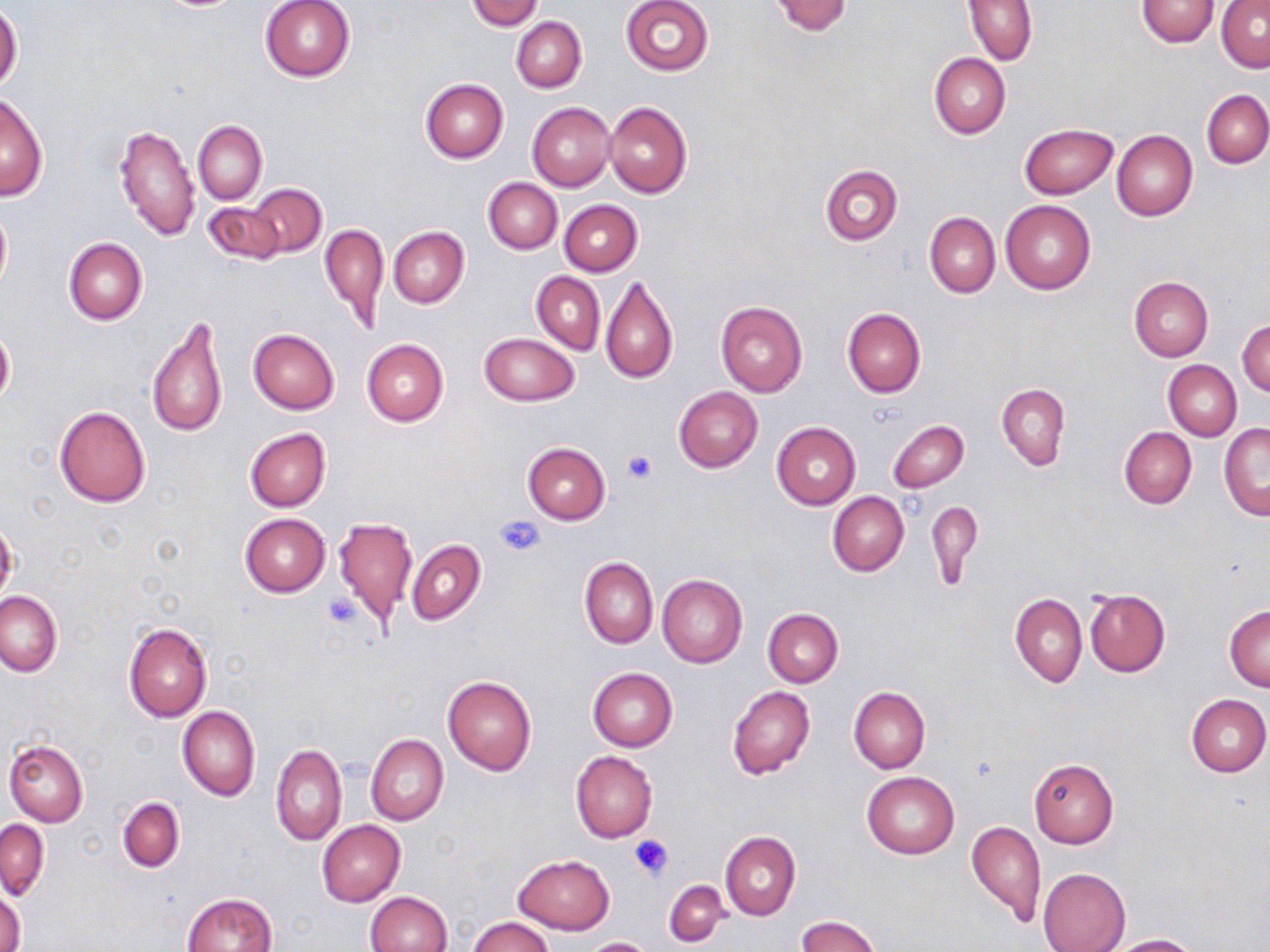

{
  "slide_level_diagnosis": "negative for blood parasites",
  "magnification": "1000x",
  "uninfected_red_blood_cell_locations": "approximate bounding boxes as (x1, y1, x2, y2) in pixels: (259, 0, 356, 82), (467, 0, 541, 29), (621, 0, 713, 75), (769, 0, 853, 36), (964, 0, 1037, 65), (1136, 0, 1219, 46), (1217, 0, 1270, 74), (0, 5, 22, 94), (512, 16, 586, 92), (929, 52, 1011, 138), (421, 79, 508, 163), (1201, 90, 1270, 168), (1, 94, 48, 201), (605, 101, 691, 198), (528, 102, 616, 191), (194, 120, 266, 205), (112, 122, 199, 242), (1019, 122, 1118, 198), (1112, 131, 1198, 222), (820, 163, 902, 244), (483, 178, 561, 254), (249, 184, 326, 258), (559, 199, 641, 276), (203, 200, 284, 266), (1001, 201, 1095, 294), (0, 206, 11, 297), (925, 212, 1000, 299), (320, 222, 388, 333), (388, 226, 469, 308), (63, 238, 147, 325), (531, 272, 605, 353), (601, 275, 678, 384), (1129, 277, 1213, 362), (715, 302, 807, 397), (842, 307, 925, 398), (146, 313, 228, 441), (1237, 318, 1270, 398), (0, 324, 15, 409), (247, 328, 339, 414), (480, 331, 579, 407), (362, 338, 448, 427), (1164, 360, 1241, 441), (996, 383, 1069, 470), (674, 387, 762, 472), (54, 406, 150, 507), (887, 420, 969, 493), (771, 422, 860, 509), (1218, 424, 1269, 520), (1119, 427, 1196, 509), (245, 429, 330, 511), (522, 442, 610, 523), (827, 492, 909, 577), (925, 499, 983, 589), (240, 513, 330, 596), (333, 517, 417, 625), (0, 520, 18, 604), (407, 539, 485, 624), (579, 557, 658, 648), (657, 574, 747, 668), (1084, 588, 1170, 677), (0, 591, 62, 676), (1011, 593, 1086, 687), (1225, 606, 1270, 691), (762, 608, 844, 688), (123, 621, 212, 721), (587, 668, 677, 751), (442, 676, 536, 775), (727, 686, 814, 780), (847, 687, 931, 772), (1186, 694, 1270, 777), (177, 706, 259, 801), (366, 734, 448, 826), (3, 739, 87, 826), (271, 744, 347, 847), (571, 751, 658, 843), (1029, 758, 1118, 847), (861, 771, 959, 859), (117, 798, 185, 872), (1, 820, 49, 900), (318, 820, 405, 906), (967, 820, 1046, 928), (720, 831, 800, 921), (512, 853, 614, 934), (1037, 867, 1131, 952), (664, 879, 729, 947), (0, 891, 25, 952), (366, 891, 451, 952), (182, 892, 278, 952), (797, 915, 881, 952), (468, 916, 553, 952), (1103, 933, 1200, 951), (582, 937, 656, 951)",
  "image_size": "1270×952 pixels",
  "stain": "May-Grünwald-Giemsa",
  "preparation": "thin blood smear",
  "modality": "light microscopy",
  "platelet_locations": "approximate bounding boxes as (x1, y1, x2, y2) in pixels: (622, 449, 656, 483), (495, 512, 544, 558), (321, 590, 361, 628), (631, 834, 673, 880)",
  "field_of_view": "one of a larger specimen"
}